Report the malaria status of this cell.
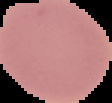

Uninfected.

preparation = thin blood smear
image size = 112×103 pixels
image type = segmented cell region with the area outside set to black